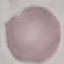

Result: no malaria parasites detected. Giemsa stain. Thin blood smear. Acquired by smartphone through the microscope eyepiece. Cell patch, automatically extracted from a larger field of view and resized to 64 × 64 pixels.